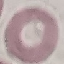
Result: no malaria parasites seen. Thin blood film. Giemsa stain. Automatically extracted cell patch, resized to 64 × 64 pixels. Photographed with a smartphone camera at the microscope eyepiece.